Assess the morphology of the red blood cells.
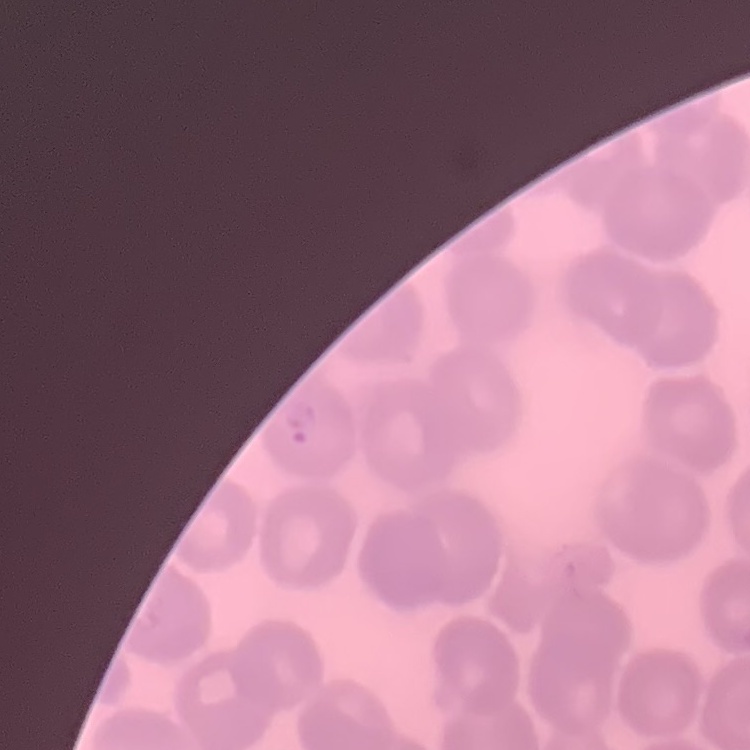
No rouleaux formation.

One tile cut from a larger photomicrograph. Field's or Giemsa stain. Thin peripheral smear.